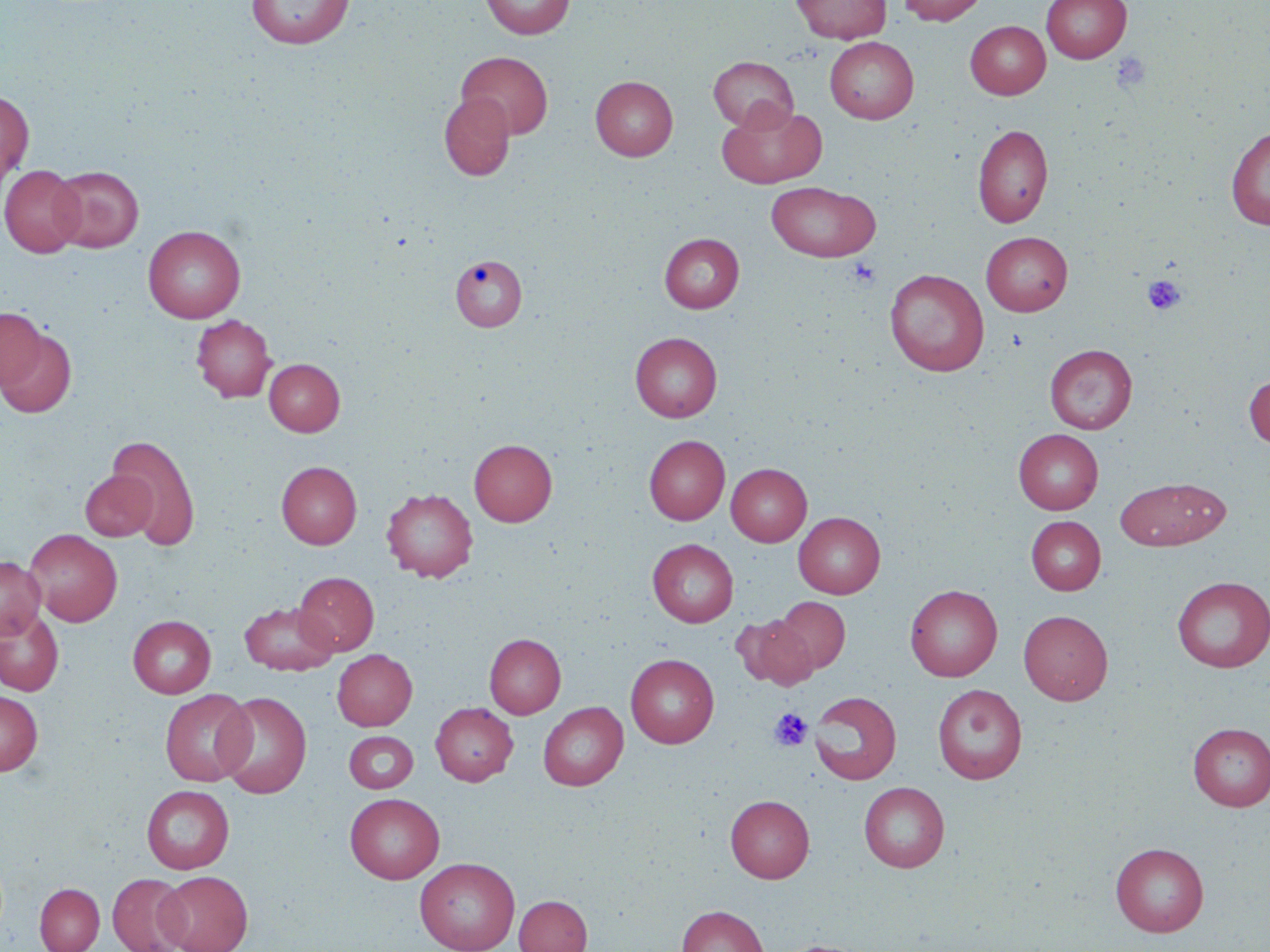

slide_level_diagnosis: no evidence of blood parasites
magnification: 1000x
uninfected_red_blood_cell_locations: 'approximate bounding boxes as (x1,y1)-(x2,y2) corner pairs in pixels: (246,0)-(354,49), (480,0)-(574,39), (791,0)-(891,43), (898,0)-(988,25), (1042,0)-(1131,63), (965,21)-(1050,99), (825,37)-(919,123), (456,51)-(553,140), (709,56)-(798,132), (591,76)-(677,160), (0,91)-(34,186), (439,92)-(515,180), (717,102)-(827,188), (973,124)-(1054,227), (1226,125)-(1270,230), (0,164)-(84,257), (50,166)-(143,252), (766,181)-(881,262), (143,225)-(245,323), (981,232)-(1073,316), (660,233)-(744,313), (449,255)-(529,333), (885,268)-(988,376), (0,307)-(47,391), (191,314)-(276,402), (0,327)-(76,418), (630,332)-(722,422), (1044,344)-(1137,434), (264,358)-(344,435), (1244,374)-(1270,449), (1013,429)-(1103,514), (108,434)-(202,550), (644,435)-(730,525), (469,439)-(557,526), (277,461)-(361,548), (726,463)-(812,546), (80,470)-(157,541), (1115,477)-(1230,550), (382,488)-(478,582), (793,512)-(885,598), (1027,516)-(1105,594), (24,529)-(123,626), (648,539)-(738,627), (0,555)-(45,640), (293,572)-(379,656), (1173,575)-(1270,672), (905,584)-(1002,681), (773,597)-(850,675), (240,602)-(338,675), (0,608)-(64,696), (1019,610)-(1113,704), (128,615)-(216,698), (734,617)-(818,689), (484,634)-(566,718), (332,649)-(417,730), (625,654)-(719,748), (932,684)-(1027,784), (160,689)-(255,786), (0,691)-(43,775), (215,691)-(312,798), (809,691)-(902,785), (431,702)-(518,785), (538,702)-(628,790), (1187,722)-(1270,811), (343,730)-(419,795), (859,781)-(949,873), (141,785)-(234,873), (344,793)-(444,883), (725,794)-(814,882), (1110,842)-(1209,936), (415,857)-(519,952), (157,870)-(253,952), (107,873)-(191,952), (35,883)-(104,952), (514,895)-(592,952), (676,904)-(768,952), (773,939)-(877,952)'
stain: May-Grünwald-Giemsa
preparation: thin blood smear
platelet_locations: 'approximate bounding boxes as (x1,y1)-(x2,y2) corner pairs in pixels: (1112,51)-(1151,92), (848,258)-(881,288), (1142,274)-(1186,315), (769,708)-(813,752)'
field_of_view: single
image_size: 1270×952 pixels
modality: light microscopy